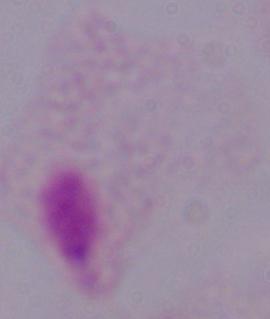

identification = trichomonad
magnification = 1000x
modality = photomicrograph